State which parasite is depicted.
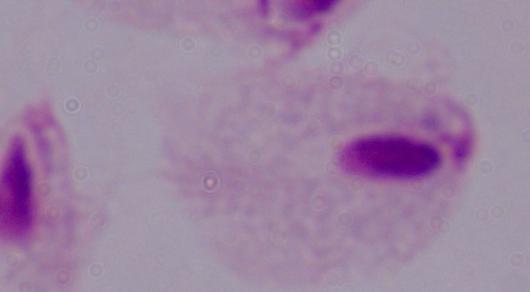

A trichomonad.

magnification = 1000x
modality = micrograph